Assess this cell for malaria.
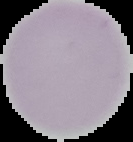
Uninfected.

preparation = thin blood film
image type = segmented cell region on a black background
image size = 133×142 pixels